State the blood parasite species.
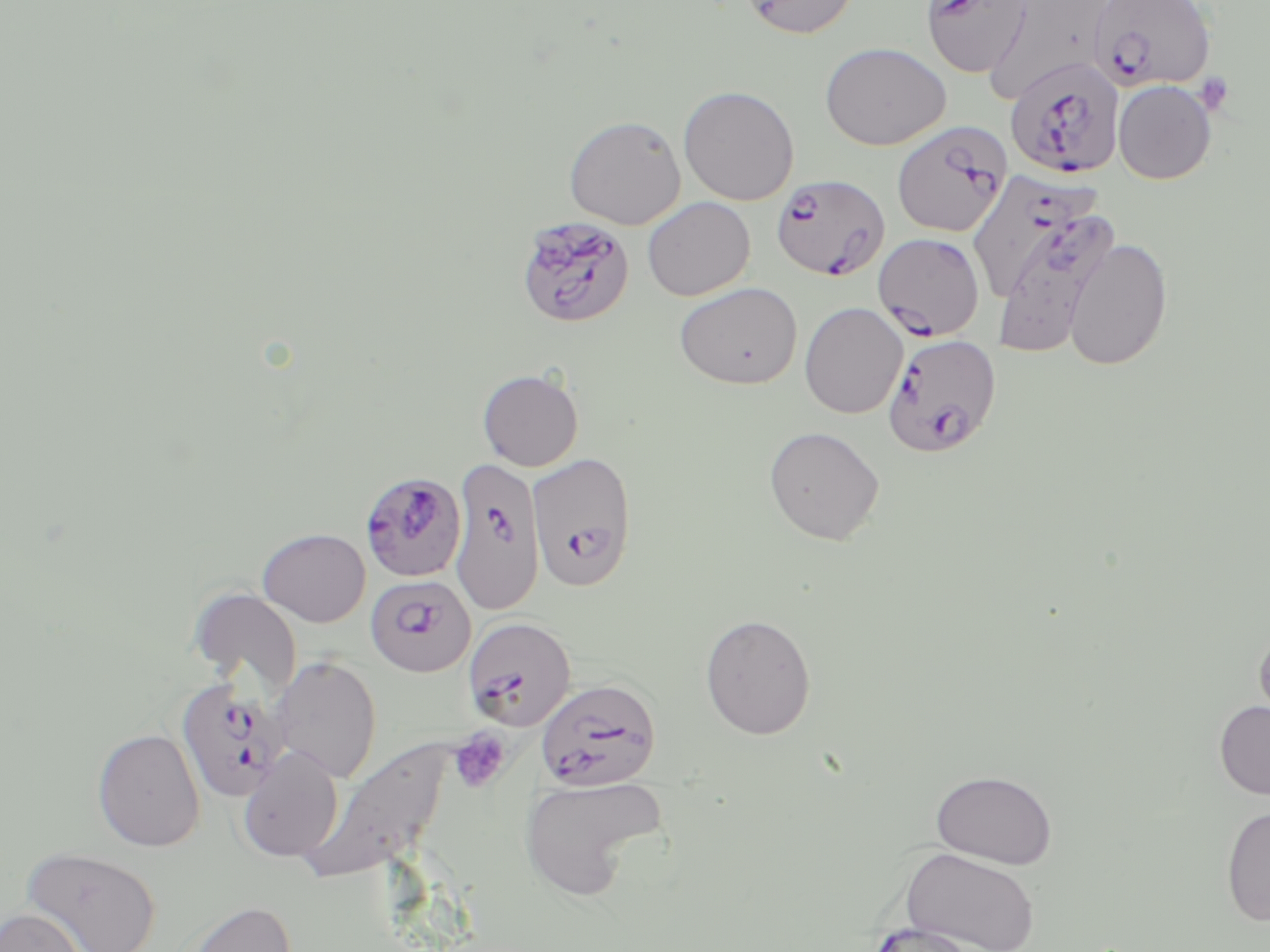

Plasmodium falciparum.

{
  "stain": "May-Grünwald-Giemsa",
  "modality": "light microscopy",
  "preparation": "thin blood smear",
  "platelet_locations": "approximate bounding boxes as named x1/y1/x2/y2 corners in pixels: (x1=1193, y1=72, x2=1236, y2=116), (x1=449, y1=729, x2=510, y2=793)",
  "image_size": "1270×952 pixels",
  "magnification": "1000x",
  "uninfected_red_blood_cell_locations": "approximate bounding boxes as named x1/y1/x2/y2 corners in pixels: (x1=990, y1=0, x2=1104, y2=101), (x1=738, y1=1, x2=861, y2=39), (x1=820, y1=42, x2=951, y2=151), (x1=1114, y1=80, x2=1216, y2=184), (x1=678, y1=85, x2=799, y2=205), (x1=564, y1=115, x2=686, y2=229), (x1=642, y1=196, x2=755, y2=300), (x1=1063, y1=238, x2=1173, y2=371), (x1=674, y1=282, x2=803, y2=390), (x1=799, y1=302, x2=908, y2=419), (x1=477, y1=368, x2=583, y2=471), (x1=763, y1=425, x2=885, y2=544), (x1=257, y1=527, x2=371, y2=627), (x1=188, y1=587, x2=303, y2=694), (x1=699, y1=613, x2=817, y2=739), (x1=1252, y1=624, x2=1270, y2=739), (x1=270, y1=656, x2=382, y2=783), (x1=1214, y1=700, x2=1270, y2=800), (x1=92, y1=728, x2=205, y2=852), (x1=302, y1=739, x2=453, y2=885), (x1=237, y1=746, x2=344, y2=862), (x1=931, y1=769, x2=1058, y2=868), (x1=518, y1=774, x2=668, y2=902), (x1=1220, y1=806, x2=1270, y2=926), (x1=19, y1=846, x2=163, y2=952), (x1=900, y1=847, x2=1041, y2=952), (x1=177, y1=900, x2=297, y2=952), (x1=0, y1=907, x2=87, y2=952), (x1=863, y1=921, x2=990, y2=951)",
  "field_of_view": "one of a larger specimen",
  "plasmodium_falciparum_infected_red_blood_cell_locations": "approximate bounding boxes as named x1/y1/x2/y2 corners in pixels: (x1=921, y1=0, x2=1032, y2=79), (x1=1087, y1=1, x2=1216, y2=93), (x1=1004, y1=58, x2=1124, y2=180), (x1=892, y1=120, x2=1011, y2=237), (x1=977, y1=172, x2=1098, y2=299), (x1=772, y1=174, x2=890, y2=281), (x1=1000, y1=215, x2=1121, y2=354), (x1=516, y1=216, x2=636, y2=328), (x1=874, y1=232, x2=986, y2=341), (x1=882, y1=333, x2=1002, y2=456), (x1=527, y1=451, x2=637, y2=591), (x1=450, y1=457, x2=544, y2=614), (x1=364, y1=471, x2=463, y2=578), (x1=366, y1=574, x2=476, y2=677), (x1=462, y1=616, x2=577, y2=731), (x1=175, y1=677, x2=290, y2=802), (x1=535, y1=677, x2=662, y2=791)"
}